Give the extent of all Plasmodium falciparum-infected red blood cells.
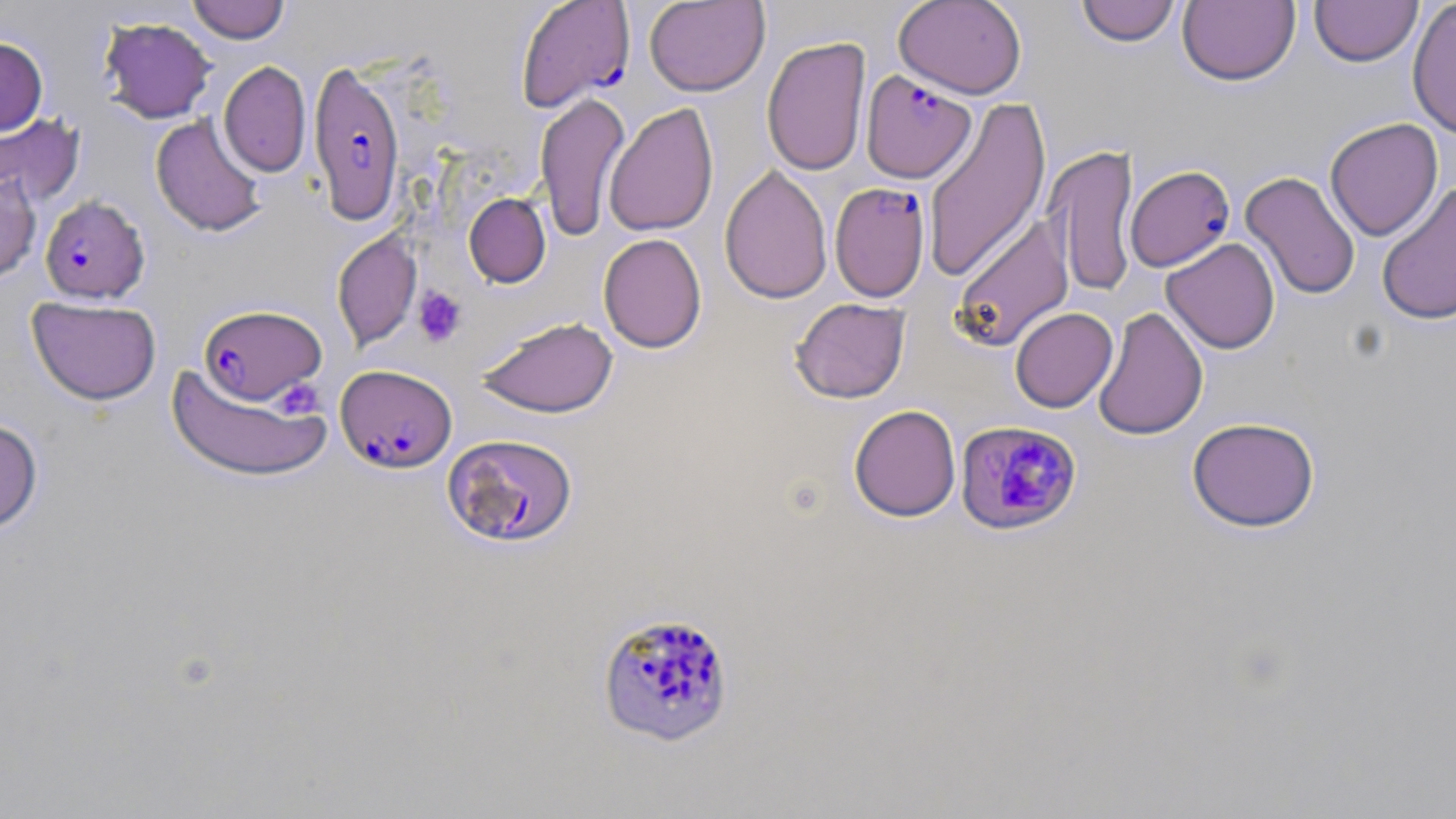

Approximate bounding boxes as (x1,y1)-(x2,y2) corner pairs in pixels.
Plasmodium falciparum-infected red blood cells: (515,1)-(635,111), (308,59)-(406,227), (861,70)-(975,183), (1125,164)-(1235,271), (830,181)-(931,302), (40,195)-(149,304), (198,305)-(326,405), (336,365)-(456,473), (955,420)-(1083,536), (443,434)-(578,548), (596,610)-(735,748).

Summary:
  - Platelet locations: (413,286)-(467,347), (275,379)-(324,418)
  - Uninfected red blood cell locations: (188,0)-(290,43), (643,0)-(770,97), (894,0)-(1027,99), (1178,0)-(1300,86), (1407,0)-(1456,140), (1075,1)-(1182,47), (1309,1)-(1423,67), (99,17)-(216,123), (762,36)-(871,176), (0,37)-(48,136), (218,61)-(311,177), (535,92)-(630,242), (922,95)-(1052,285), (605,103)-(719,237), (0,113)-(85,207), (150,114)-(267,237), (1324,118)-(1443,241), (1044,144)-(1141,299), (719,164)-(833,304), (0,168)-(42,283), (1240,171)-(1361,300), (1376,180)-(1456,326), (464,193)-(550,288), (951,214)-(1075,351), (332,231)-(422,350), (598,233)-(707,353), (1161,237)-(1281,354), (27,296)-(161,405), (790,298)-(911,403), (1093,306)-(1208,441), (1010,307)-(1118,412), (477,316)-(619,418), (166,363)-(332,483), (849,404)-(961,522), (1187,416)-(1320,532), (0,418)-(43,533)
  - Slide-level diagnosis: Plasmodium falciparum
  - Stain: May-Grünwald-Giemsa
  - Field of view: one of a larger specimen
  - Preparation: thin blood smear
  - Modality: optical microscopy
  - Image size: 1456×819 pixels
  - Magnification: 1000x